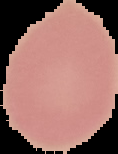
Summary:
  - Preparation: thin blood smear
  - Image type: segmented cell region with the area outside set to black
  - Result: no Plasmodium parasites detected
  - Image size: 118×154 pixels